Locate and identify every blood parasite.
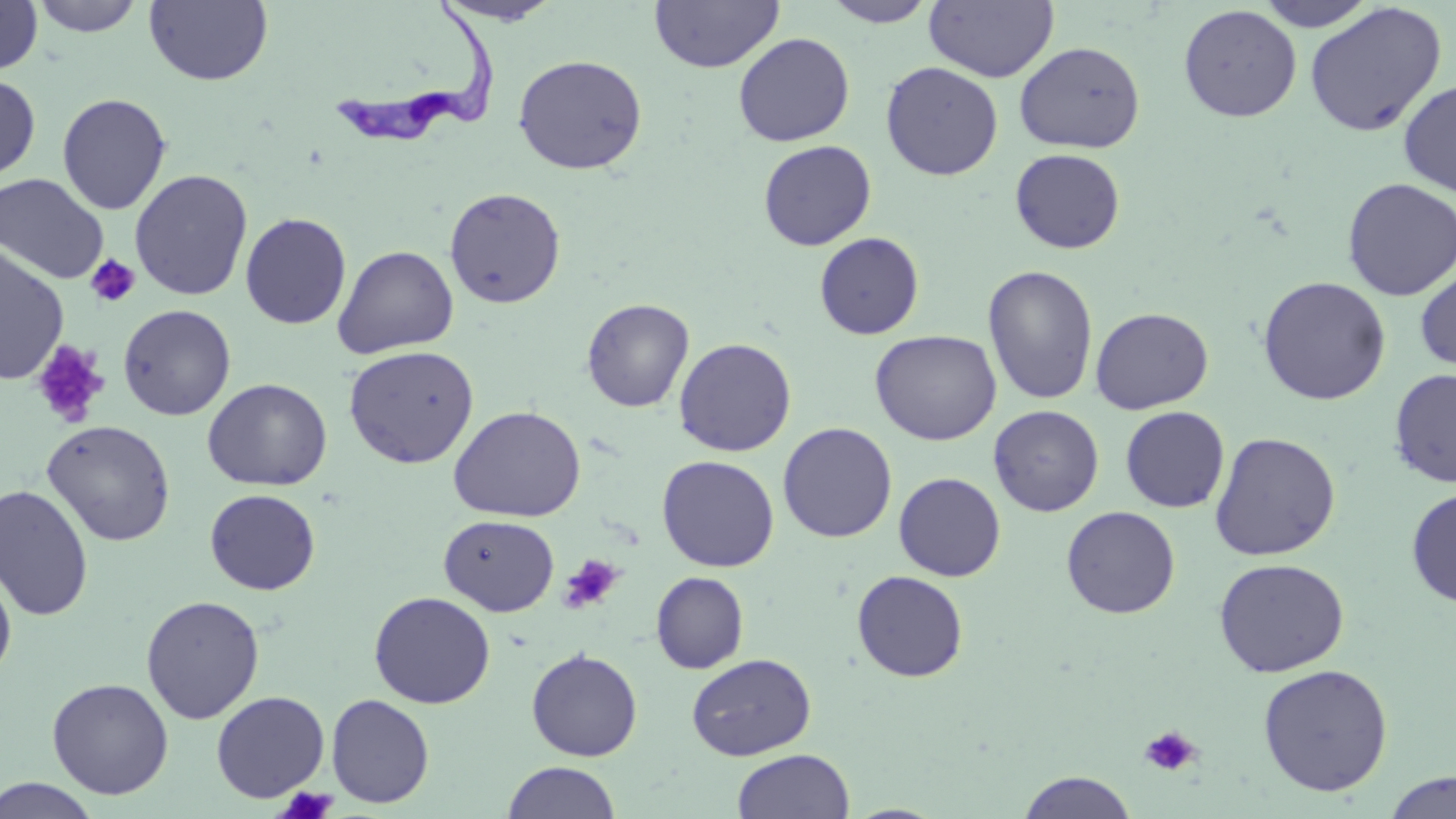
Approximate bounding boxes as (x1, y1, x2, y2) in pixels.
Trypanosoma brucei: (330, 4, 501, 148).
No Plasmodium falciparum, Plasmodium ovale, Plasmodium malariae, Plasmodium vivax, or Babesia divergens observed.

slide_level_diagnosis: Trypanosoma brucei
image_size: 1456×819 pixels
preparation: thin blood film
modality: light microscopy
magnification: 1000x
stain: May-Grünwald-Giemsa
platelet_locations: 'approximate bounding boxes as (x1, y1, x2, y2) in pixels: (85, 255, 140, 307), (32, 340, 109, 427), (558, 554, 623, 615), (1139, 725, 1200, 777), (277, 786, 337, 819)'
uninfected_red_blood_cell_locations: 'approximate bounding boxes as (x1, y1, x2, y2) in pixels: (0, 0, 43, 75), (30, 0, 146, 37), (144, 0, 273, 86), (648, 0, 785, 73), (925, 0, 1059, 82), (1255, 0, 1379, 31), (431, 1, 563, 26), (821, 1, 938, 27), (1304, 2, 1447, 137), (1178, 5, 1301, 122), (733, 32, 855, 146), (1014, 41, 1145, 154), (512, 54, 648, 175), (880, 61, 1004, 181), (0, 73, 41, 184), (1398, 79, 1456, 197), (56, 92, 172, 215), (757, 140, 877, 251), (1009, 148, 1126, 254), (129, 168, 253, 301), (0, 172, 110, 285), (1341, 178, 1455, 301), (444, 187, 566, 309), (240, 212, 352, 329), (814, 232, 925, 340), (0, 243, 69, 386), (333, 244, 459, 358), (1415, 263, 1456, 375), (982, 264, 1099, 405), (1257, 276, 1392, 405), (582, 298, 694, 412), (118, 304, 236, 420), (1090, 307, 1214, 414), (870, 329, 1001, 446), (673, 337, 797, 457), (344, 345, 479, 469), (1389, 368, 1456, 487), (203, 378, 332, 491), (448, 405, 586, 522), (989, 405, 1104, 516), (1120, 406, 1230, 513), (42, 421, 176, 545), (778, 422, 897, 542), (1209, 431, 1341, 561), (657, 455, 779, 572), (894, 472, 1006, 582), (0, 484, 94, 621), (1406, 486, 1456, 608), (205, 488, 320, 594), (1061, 505, 1181, 618), (438, 515, 559, 616), (1213, 557, 1349, 677), (0, 564, 17, 682), (852, 570, 969, 683), (651, 571, 749, 674), (369, 591, 496, 708), (140, 595, 265, 724), (526, 648, 643, 761), (686, 652, 816, 760), (1257, 663, 1394, 797), (46, 677, 174, 799), (211, 690, 330, 802), (326, 693, 435, 808), (731, 748, 855, 819), (501, 761, 621, 819), (1017, 770, 1138, 818), (1383, 771, 1456, 819), (1, 777, 102, 818)'
field_of_view: one of a larger specimen